Point out each Plasmodium parasite.
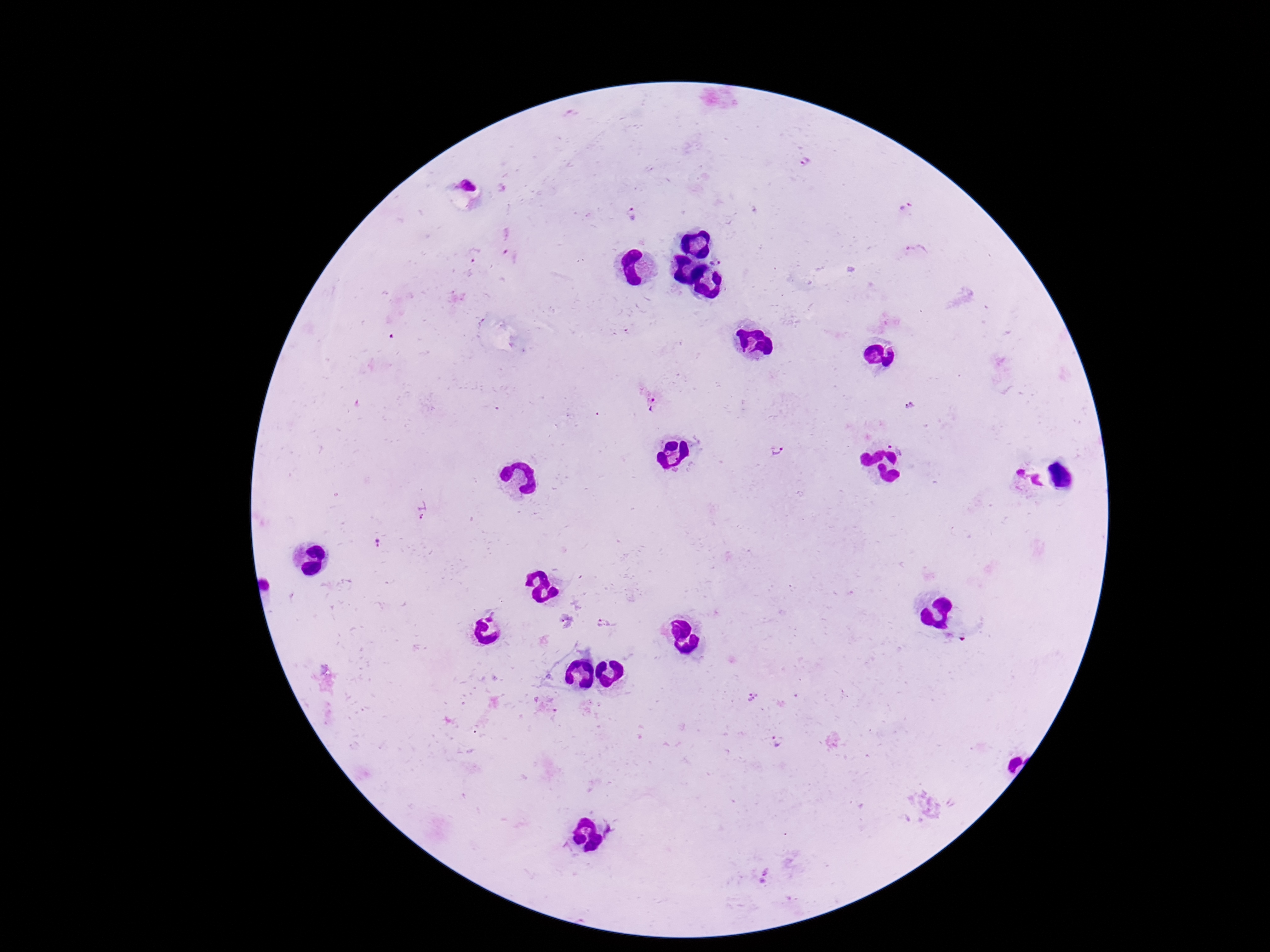
Approximate centers as (x, y) in pixels.
Plasmodium parasites: (805, 161), (905, 207), (631, 213), (918, 253), (717, 258), (651, 403), (908, 406), (899, 443), (778, 450), (424, 509), (380, 543), (606, 625), (776, 743).

field of view = one from this slide
image size = 1270×952 pixels
patient malaria status = positive
stain = Giemsa
preparation = thick peripheral-blood smear
magnification = 100x
capture = smartphone camera through the microscope eyepiece